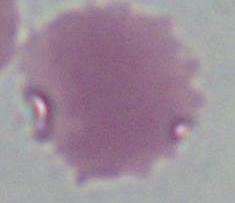

magnification = 1000x
identification = red blood cell
modality = micrograph